Describe the morphology of the red blood cells.
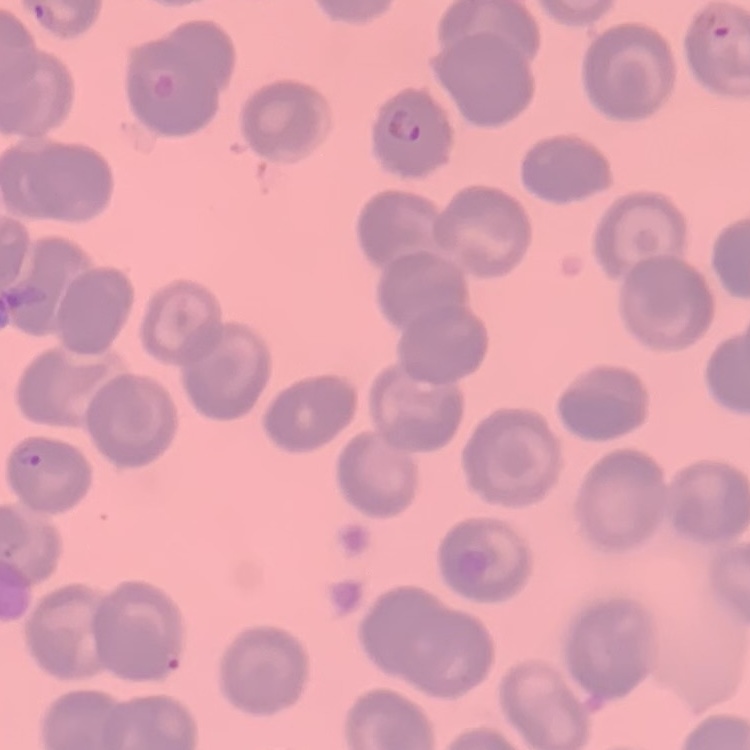

They show no rouleaux formation.

One tile cut from a larger photomicrograph. Thin blood film. Stained with either Field's or Giemsa.